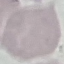
malaria status = uninfected
image type = cell patch, automatically extracted from a larger field of view and resized to 64 × 64 pixels
capture = smartphone camera at the microscope eyepiece
preparation = thin smear
stain = Giemsa